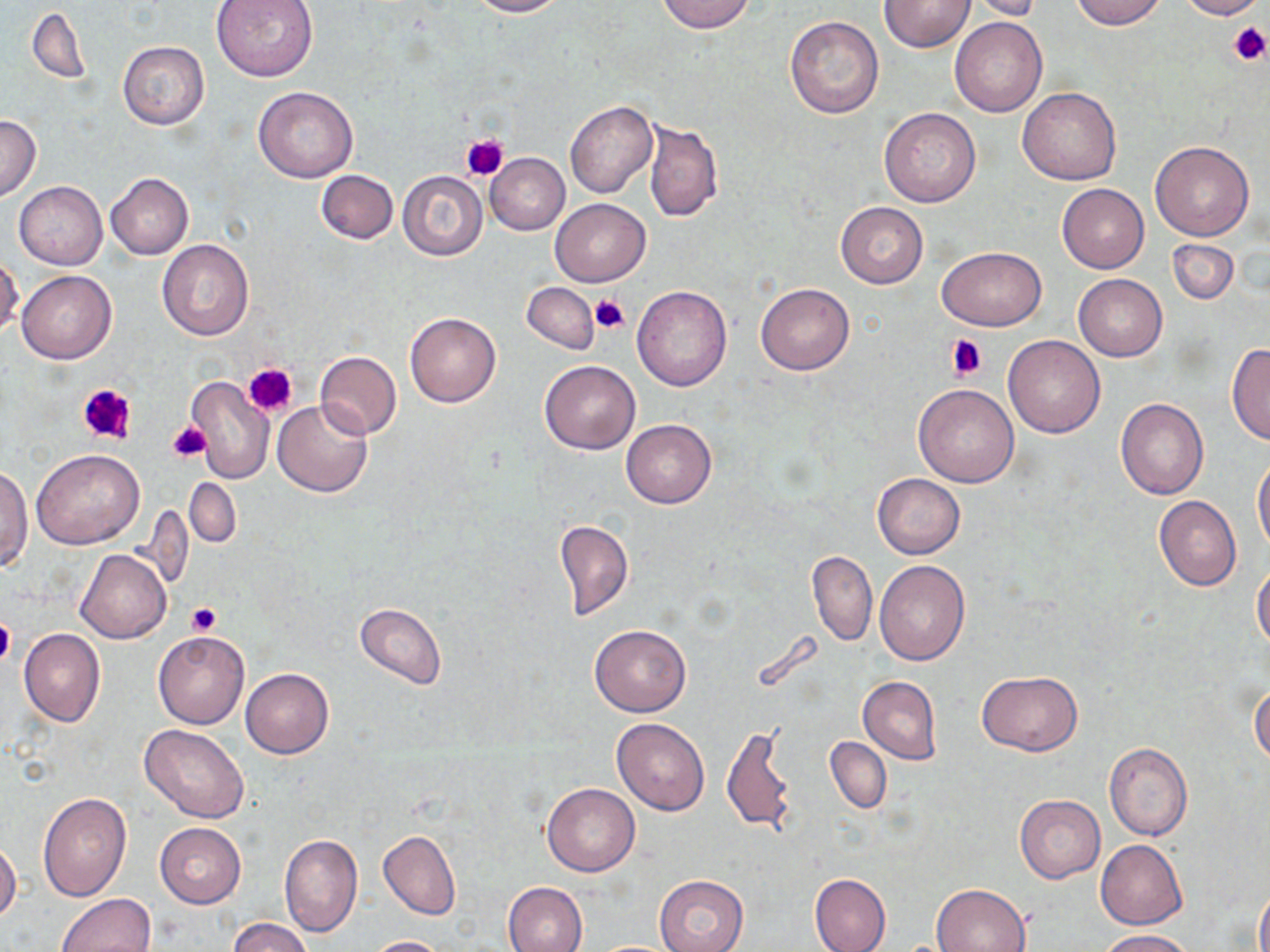
slide-level diagnosis = negative for blood parasites
preparation = thin blood smear
field of view = one of a larger specimen
uninfected red blood cell locations = approximate bounding boxes as [x1, y1, x2, y2] in pixels: [210, 0, 317, 81], [465, 0, 565, 17], [656, 0, 757, 33], [880, 0, 975, 51], [1070, 0, 1167, 29], [1177, 0, 1265, 20], [970, 1, 1046, 20], [28, 7, 90, 84], [785, 16, 884, 119], [949, 16, 1048, 117], [117, 41, 209, 131], [253, 86, 358, 183], [1017, 87, 1121, 185], [564, 100, 657, 198], [878, 107, 982, 207], [0, 114, 42, 201], [643, 118, 722, 223], [1150, 141, 1254, 241], [485, 152, 570, 234], [315, 170, 398, 244], [397, 171, 488, 261], [105, 173, 194, 259], [13, 181, 107, 270], [1057, 184, 1149, 273], [550, 199, 650, 286], [835, 202, 928, 288], [1167, 238, 1239, 305], [157, 239, 256, 341], [938, 247, 1047, 330], [0, 256, 24, 339], [17, 270, 116, 363], [1073, 274, 1168, 362], [522, 281, 599, 353], [755, 282, 854, 375], [631, 285, 733, 390], [404, 312, 501, 407], [1003, 335, 1106, 438], [1226, 344, 1269, 444], [315, 352, 402, 440], [539, 361, 641, 454], [185, 377, 274, 485], [914, 385, 1018, 487], [1116, 397, 1209, 500], [273, 399, 373, 497], [620, 420, 716, 508], [32, 450, 143, 548], [1253, 454, 1270, 554], [1, 464, 32, 571], [872, 474, 965, 559], [185, 477, 242, 548], [1154, 496, 1241, 591], [554, 518, 633, 621], [74, 550, 171, 643], [808, 551, 877, 646], [875, 560, 970, 665], [1252, 566, 1270, 649], [355, 603, 447, 689], [589, 623, 692, 717], [19, 629, 105, 726], [153, 630, 249, 729], [240, 668, 333, 758], [978, 670, 1082, 756], [858, 676, 941, 763], [1250, 683, 1270, 765], [612, 717, 710, 815], [723, 723, 797, 837], [140, 724, 250, 823], [825, 737, 890, 815], [1103, 742, 1192, 841], [542, 782, 640, 877], [38, 792, 131, 901], [1014, 795, 1105, 883], [154, 822, 246, 907], [378, 829, 460, 920], [279, 833, 363, 937], [1096, 840, 1187, 929], [0, 841, 21, 924], [809, 873, 890, 952], [656, 874, 749, 952], [502, 882, 587, 952], [931, 882, 1031, 951], [1255, 883, 1270, 952], [56, 893, 156, 952], [228, 917, 313, 952], [1099, 929, 1197, 951], [365, 935, 450, 952]
modality = light microscopy
stain = May-Grünwald-Giemsa
platelet locations = approximate bounding boxes as [x1, y1, x2, y2] in pixels: [1227, 20, 1270, 65], [459, 132, 509, 182], [589, 294, 629, 334], [945, 334, 987, 380], [244, 362, 296, 416], [75, 383, 138, 445], [166, 420, 211, 462], [187, 602, 221, 636], [0, 613, 15, 668]
magnification = 1000x
image size = 1270×952 pixels